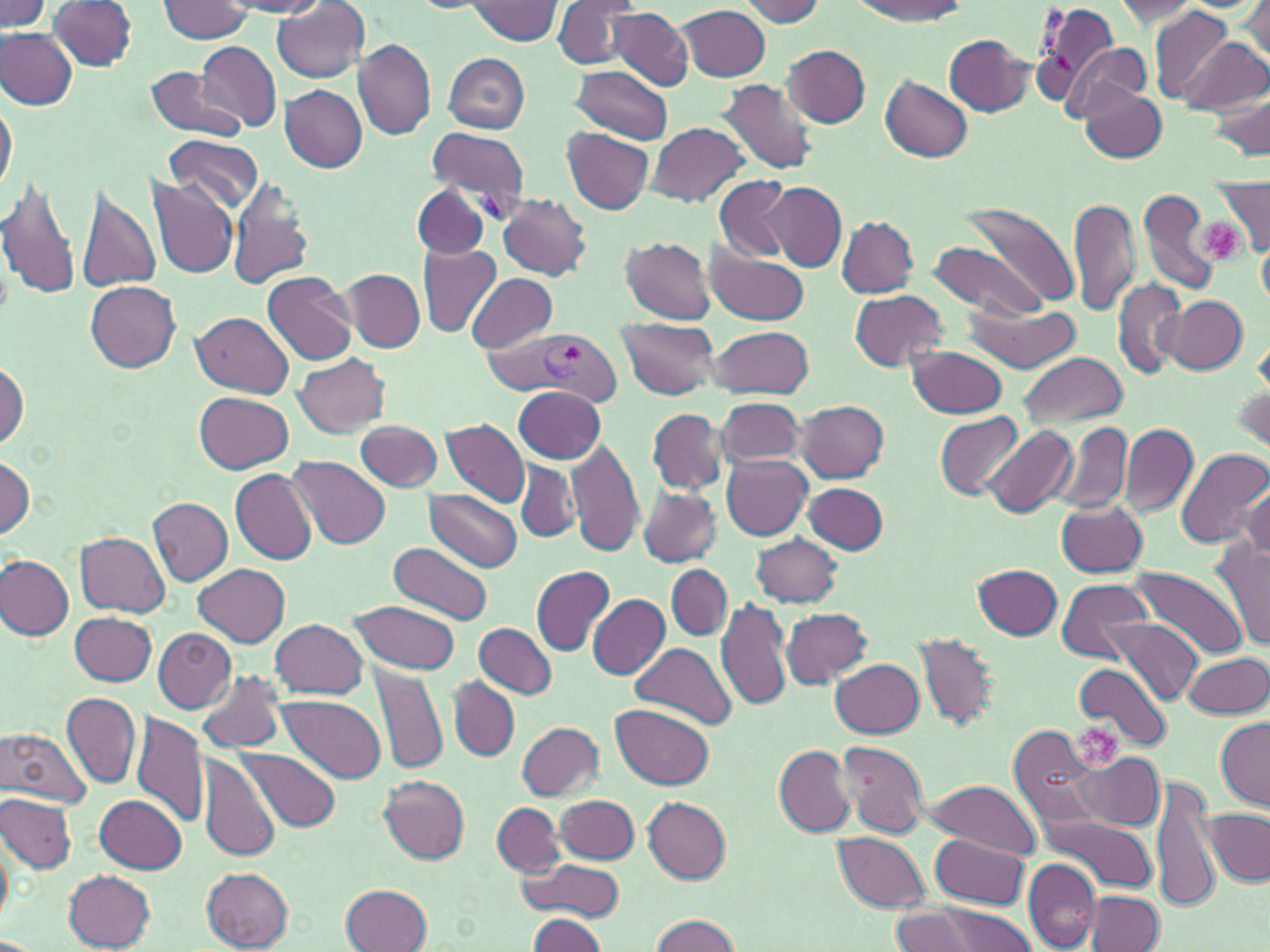

slide-level diagnosis = Plasmodium vivax
preparation = thin blood film
uninfected red blood cell locations (subset) = approximate bounding boxes as [x1, y1, x2, y2] in pixels: [0, 0, 52, 31], [552, 0, 644, 69], [738, 0, 827, 26], [850, 0, 968, 22], [158, 1, 255, 44], [225, 1, 330, 16], [465, 1, 563, 47], [1113, 1, 1201, 25], [1239, 1, 1269, 68], [49, 2, 139, 72], [272, 4, 370, 83], [679, 5, 771, 81], [1149, 7, 1235, 103], [607, 8, 692, 89], [1, 29, 77, 109], [946, 35, 1033, 116], [1178, 37, 1268, 115], [197, 39, 281, 132], [354, 39, 435, 139], [1062, 42, 1150, 122], [782, 44, 871, 129], [442, 53, 530, 133], [145, 63, 246, 144], [570, 66, 673, 143], [880, 77, 972, 162], [721, 80, 817, 178], [280, 85, 367, 173], [1207, 88, 1270, 161], [1081, 89, 1165, 162], [0, 95, 16, 198], [647, 122, 749, 207], [562, 127, 655, 214], [167, 133, 263, 214], [0, 173, 85, 302], [150, 176, 240, 278], [227, 176, 314, 290], [713, 176, 793, 263], [74, 181, 162, 297], [1210, 181, 1270, 255], [764, 183, 846, 271], [412, 184, 490, 260], [1138, 187, 1221, 299], [498, 192, 592, 280], [1070, 195, 1139, 318], [965, 202, 1080, 310], [837, 216, 918, 297], [619, 236, 717, 325], [928, 240, 1048, 322], [416, 245, 501, 338], [1258, 245, 1270, 309], [704, 246, 809, 324], [343, 268, 426, 352], [263, 271, 357, 366], [466, 273, 557, 354], [1113, 278, 1186, 378], [86, 282, 182, 372], [851, 290, 949, 371], [1161, 296, 1248, 374], [966, 304, 1085, 373], [193, 311, 293, 396], [615, 317, 722, 401], [708, 324, 813, 399], [907, 345, 1009, 417], [1018, 351, 1129, 429], [294, 352, 390, 438], [0, 358, 29, 451], [514, 386, 605, 463], [1233, 386, 1269, 454], [196, 393, 296, 474], [715, 397, 804, 470], [796, 400, 888, 481], [647, 407, 726, 495], [935, 412, 1023, 501], [442, 419, 530, 509], [356, 420, 442, 491], [1054, 420, 1133, 515], [980, 424, 1078, 518], [1119, 424, 1196, 517], [566, 436, 645, 556], [1175, 447, 1270, 550], [1, 453, 34, 539], [722, 454, 813, 541], [291, 456, 392, 549], [516, 460, 580, 542], [230, 470, 316, 564], [1241, 481, 1270, 560], [803, 483, 887, 555], [639, 487, 722, 566], [426, 490, 521, 571], [149, 498, 234, 585], [1056, 499, 1150, 578], [76, 533, 169, 615], [752, 533, 842, 607], [1211, 540, 1270, 652], [391, 542, 492, 624], [0, 555, 73, 641], [195, 564, 289, 647], [666, 564, 732, 641], [531, 565, 616, 656], [974, 565, 1063, 641], [1129, 567, 1246, 658], [1055, 579, 1150, 664], [587, 595, 670, 680], [716, 598, 793, 713], [349, 601, 463, 674], [780, 607, 873, 686], [71, 611, 156, 687], [1104, 617, 1202, 706], [270, 618, 369, 700], [473, 622, 558, 699], [153, 629, 236, 711], [913, 633, 1000, 731], [631, 641, 736, 729], [1185, 651, 1268, 719], [831, 658, 925, 736], [1073, 662, 1170, 753], [370, 665, 449, 777], [197, 668, 285, 753], [448, 676, 519, 762], [62, 691, 142, 789], [276, 695, 388, 783], [611, 704, 714, 790], [131, 712, 207, 830], [1215, 717, 1269, 811], [517, 721, 604, 801], [1009, 723, 1104, 831], [0, 727, 92, 807], [834, 739, 929, 839], [235, 745, 342, 833], [774, 745, 856, 836], [1072, 751, 1165, 832], [199, 753, 281, 863], [378, 776, 470, 864], [925, 777, 1042, 860], [1152, 781, 1221, 913], [1, 794, 77, 873], [95, 795, 187, 873], [555, 796, 639, 862], [643, 797, 732, 881], [493, 803, 564, 877], [1206, 808, 1267, 885], [1036, 810, 1158, 894], [0, 830, 12, 928], [832, 830, 933, 912], [930, 832, 1029, 909], [1022, 859, 1101, 952], [526, 860, 626, 922], [202, 867, 294, 952], [64, 871, 156, 951], [341, 884, 432, 952], [1084, 892, 1165, 951], [921, 902, 1040, 951], [890, 904, 992, 952], [527, 914, 607, 952], [650, 914, 741, 951]
platelet locations = approximate bounding boxes as [x1, y1, x2, y2] in pixels: [1198, 218, 1246, 266], [1076, 720, 1129, 773]
stain = May-Grünwald-Giemsa
modality = light microscopy
image size = 1270×952 pixels
magnification = 1000x
field of view = single